State the blood parasite species.
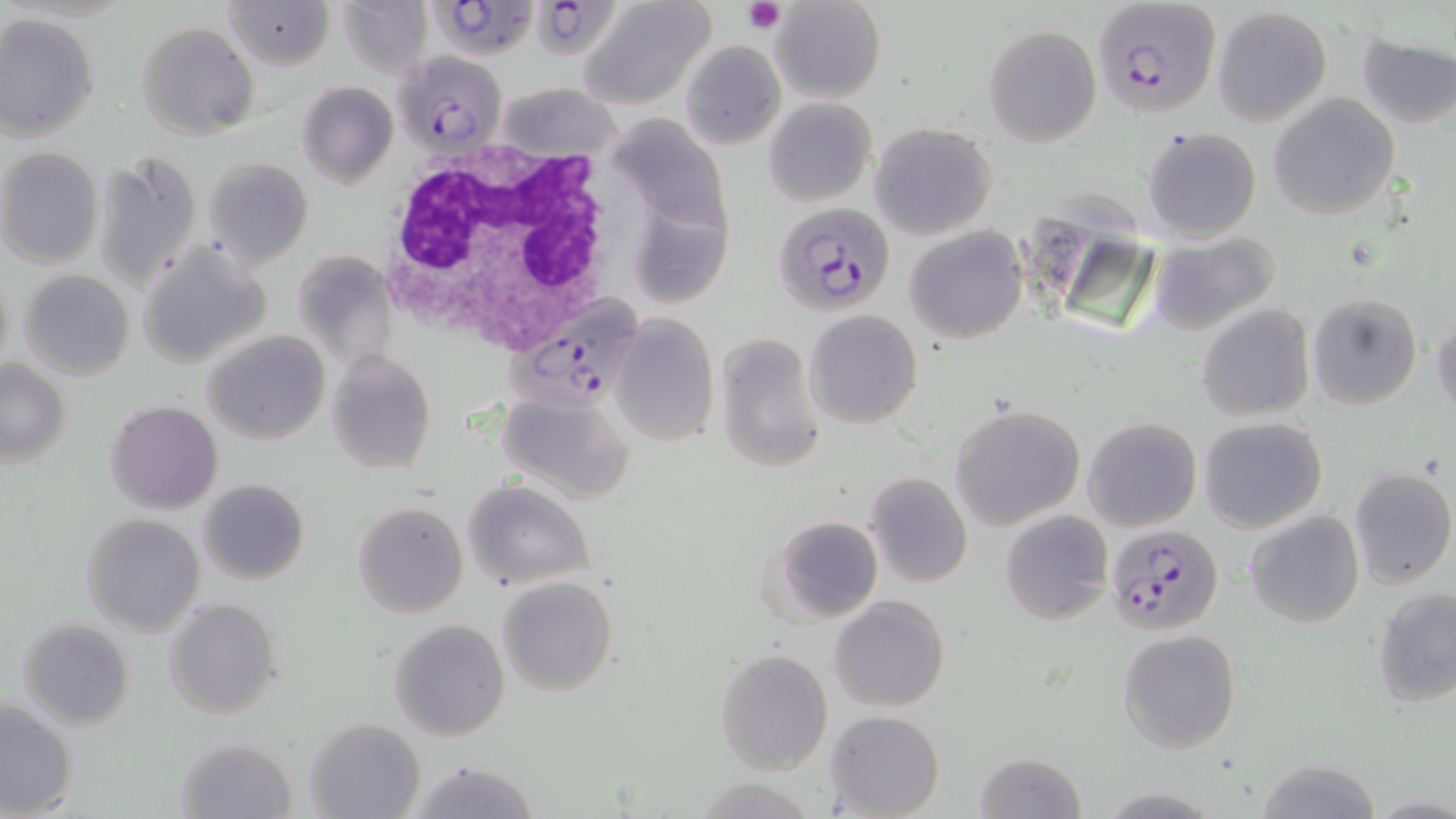
Plasmodium falciparum.

Summary:
  - Coordinate format: approximate bounding boxes as (x1, y1, x2, y2) in pixels
  - Plasmodium falciparum-infected red blood cell locations: (429, 0, 541, 58), (534, 0, 611, 55), (1090, 3, 1222, 118), (393, 52, 507, 156), (771, 201, 896, 317), (507, 295, 649, 413), (1105, 523, 1224, 635)
  - Uninfected red blood cell locations: (226, 0, 334, 70), (338, 0, 431, 77), (577, 0, 715, 109), (771, 0, 886, 103), (1212, 6, 1333, 125), (0, 14, 99, 142), (135, 20, 259, 139), (982, 23, 1101, 147), (1355, 32, 1456, 129), (680, 40, 786, 149), (297, 81, 398, 188), (499, 81, 622, 161), (1269, 93, 1399, 220), (763, 97, 877, 207), (614, 112, 735, 241), (869, 121, 998, 239), (1142, 126, 1262, 244), (0, 147, 103, 269), (95, 149, 202, 286), (207, 154, 315, 269), (642, 205, 737, 310), (905, 225, 1026, 345), (1146, 231, 1284, 337), (139, 242, 269, 368), (294, 249, 397, 373), (0, 264, 14, 376), (19, 269, 135, 380), (1307, 291, 1423, 410), (1196, 304, 1315, 421), (803, 311, 923, 429), (1430, 314, 1456, 418), (611, 316, 718, 447), (203, 330, 330, 444), (716, 330, 827, 474), (327, 348, 438, 475), (0, 361, 70, 466), (498, 394, 635, 504), (106, 399, 224, 515), (949, 403, 1087, 531), (1083, 416, 1201, 532), (1197, 416, 1328, 532), (1347, 467, 1456, 589), (865, 473, 973, 589), (197, 477, 310, 585), (463, 479, 595, 589), (353, 501, 468, 618), (999, 510, 1114, 626), (1245, 510, 1364, 627), (81, 513, 206, 636), (765, 515, 884, 623), (497, 576, 618, 696), (1372, 586, 1456, 710), (830, 594, 949, 711), (165, 599, 282, 719), (18, 618, 135, 729), (388, 618, 510, 740), (1118, 628, 1241, 753), (714, 648, 833, 774), (1, 701, 78, 818), (826, 707, 945, 818), (305, 717, 425, 819), (176, 737, 298, 819), (974, 751, 1088, 819), (1255, 758, 1384, 818), (403, 760, 545, 818), (1095, 785, 1227, 817), (1367, 794, 1454, 816)
  - Platelet locations: (741, 0, 783, 34)
  - White blood cell locations: (378, 132, 632, 355)
  - Field of view: one of a larger specimen
  - Stain: May-Grünwald-Giemsa
  - Preparation: thin blood film
  - Modality: optical microscopy
  - Magnification: 1000x
  - Image size: 1456×819 pixels